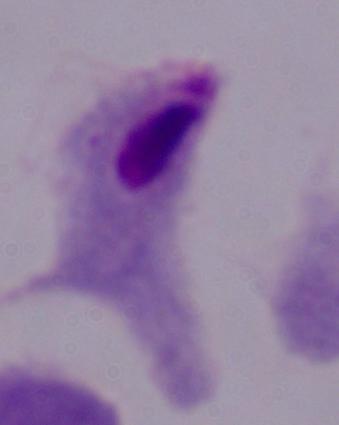
Summary:
  - Magnification: 1000x
  - Modality: photomicrograph
  - Identification: trichomonad